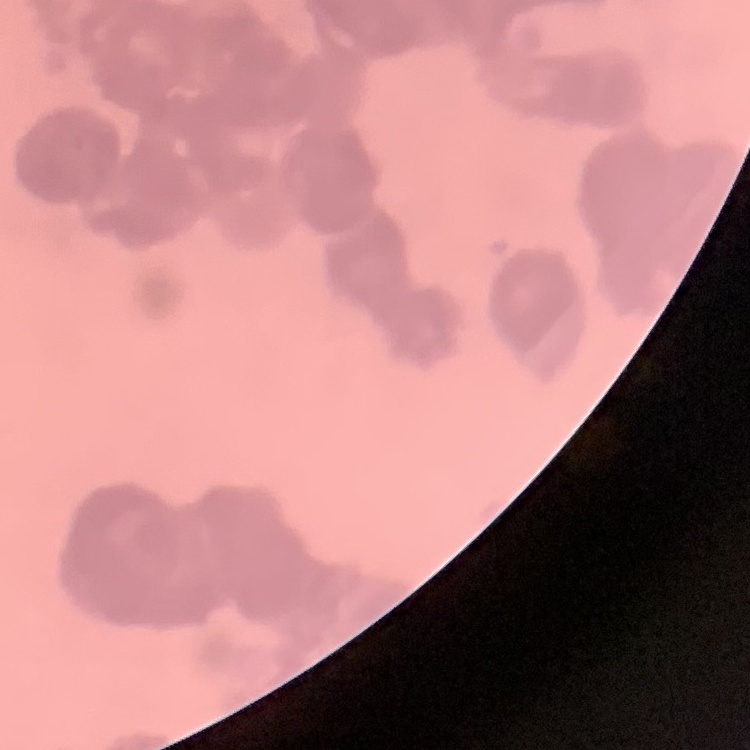
Summary:
  - Red blood cell morphology: rouleaux formation
  - Preparation: thin blood film
  - Stain: Field's or Giemsa
  - Image type: square crop of a larger photomicrograph